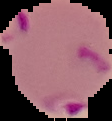 Result: Plasmodium parasites detected. From a thin blood smear. Cell region segmented out of the field of view; the surrounding area is masked to black. Image is 112×121 pixels.